Describe the morphology of the red blood cells.
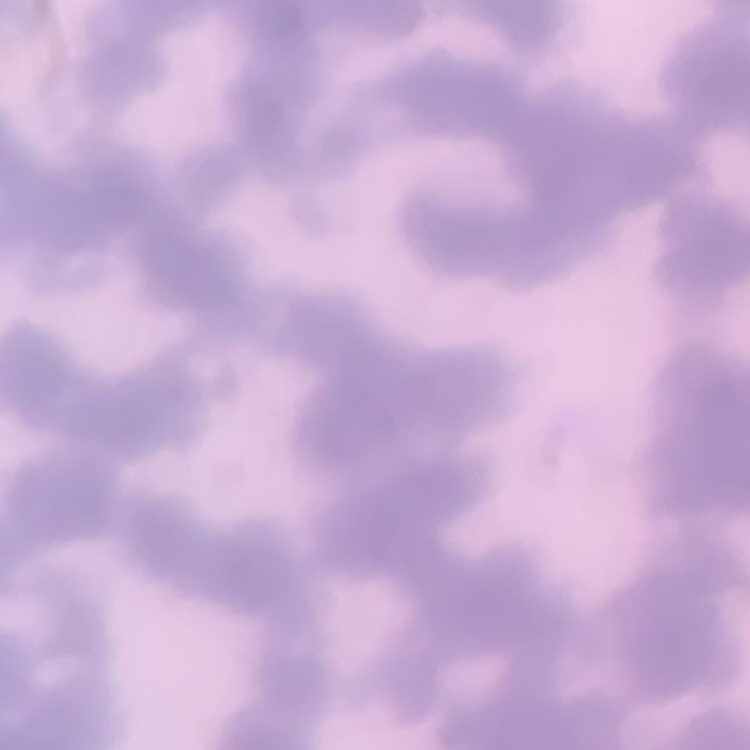

Rouleaux formation.

Thin blood smear. Field's or Giemsa stain. One tile cut from a larger photomicrograph.